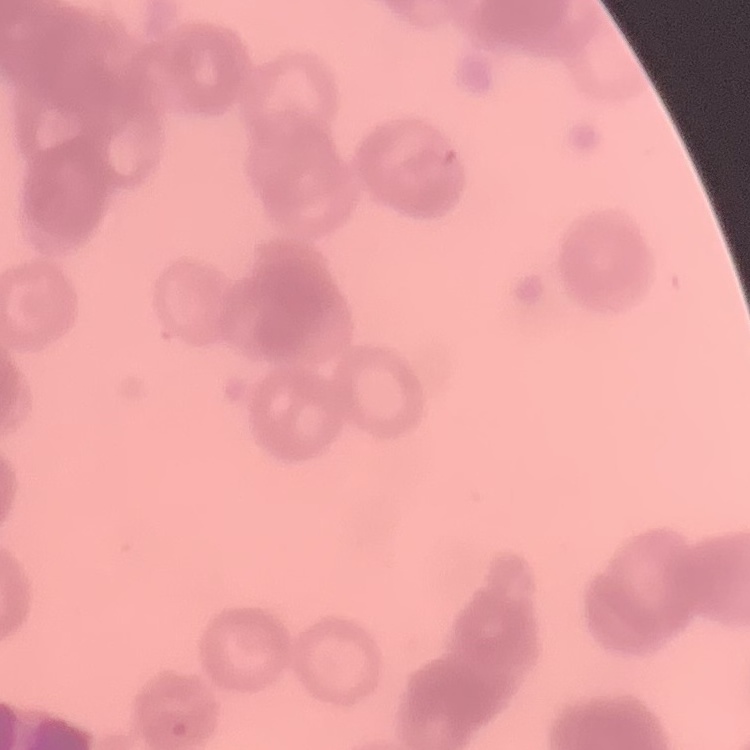

erythrocyte morphology = rouleaux formation
preparation = thin blood film
image type = square crop of a larger photomicrograph
stain = Field's or Giemsa